Mark where platelets are.
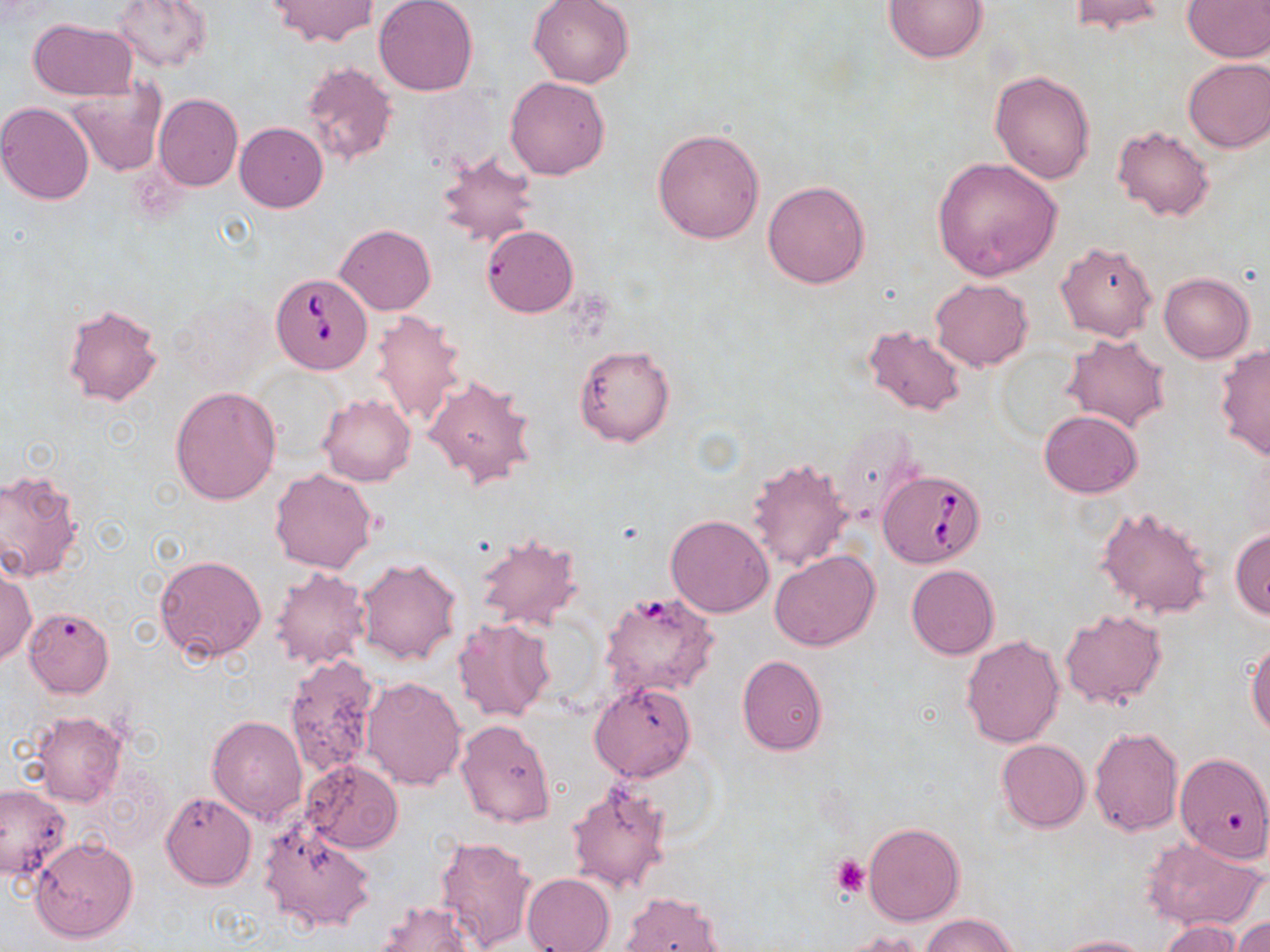
Approximate bounding boxes as named x1/y1/x2/y2 corners in pixels.
Platelets: (x1=831, y1=854, x2=871, y2=898).

Uninfected red blood cell locations: (x1=113, y1=0, x2=212, y2=71), (x1=264, y1=0, x2=378, y2=47), (x1=374, y1=0, x2=479, y2=97), (x1=528, y1=0, x2=634, y2=87), (x1=884, y1=0, x2=989, y2=64), (x1=1068, y1=0, x2=1165, y2=35), (x1=1183, y1=1, x2=1270, y2=61), (x1=28, y1=18, x2=138, y2=101), (x1=1182, y1=57, x2=1270, y2=153), (x1=302, y1=61, x2=398, y2=166), (x1=990, y1=69, x2=1095, y2=185), (x1=505, y1=76, x2=610, y2=179), (x1=64, y1=82, x2=166, y2=176), (x1=152, y1=93, x2=242, y2=191), (x1=0, y1=103, x2=96, y2=205), (x1=234, y1=122, x2=328, y2=212), (x1=1112, y1=124, x2=1214, y2=222), (x1=651, y1=127, x2=765, y2=244), (x1=432, y1=148, x2=539, y2=251), (x1=931, y1=157, x2=1062, y2=280), (x1=762, y1=180, x2=870, y2=288), (x1=337, y1=223, x2=435, y2=314), (x1=481, y1=225, x2=577, y2=317), (x1=1055, y1=240, x2=1158, y2=341), (x1=1158, y1=271, x2=1255, y2=362), (x1=931, y1=278, x2=1032, y2=370), (x1=61, y1=301, x2=162, y2=406), (x1=369, y1=309, x2=469, y2=430), (x1=862, y1=325, x2=967, y2=417), (x1=1062, y1=333, x2=1172, y2=433), (x1=1214, y1=343, x2=1270, y2=461), (x1=573, y1=345, x2=675, y2=447), (x1=423, y1=372, x2=537, y2=490), (x1=170, y1=386, x2=282, y2=506), (x1=318, y1=393, x2=416, y2=487), (x1=1040, y1=409, x2=1142, y2=498), (x1=832, y1=423, x2=924, y2=524), (x1=747, y1=457, x2=854, y2=573), (x1=269, y1=469, x2=378, y2=573), (x1=0, y1=470, x2=85, y2=582), (x1=1094, y1=504, x2=1214, y2=619), (x1=665, y1=515, x2=774, y2=618), (x1=1230, y1=528, x2=1270, y2=620), (x1=474, y1=532, x2=583, y2=629), (x1=769, y1=551, x2=879, y2=651), (x1=155, y1=554, x2=268, y2=664), (x1=355, y1=556, x2=462, y2=666), (x1=0, y1=563, x2=35, y2=666), (x1=906, y1=565, x2=999, y2=660), (x1=270, y1=567, x2=370, y2=669), (x1=598, y1=593, x2=718, y2=699), (x1=22, y1=606, x2=115, y2=699), (x1=1059, y1=609, x2=1167, y2=710), (x1=452, y1=618, x2=556, y2=723), (x1=960, y1=634, x2=1064, y2=748), (x1=1247, y1=638, x2=1270, y2=738), (x1=736, y1=655, x2=828, y2=754), (x1=284, y1=657, x2=377, y2=779), (x1=361, y1=676, x2=467, y2=791), (x1=589, y1=681, x2=696, y2=781), (x1=32, y1=711, x2=127, y2=806), (x1=207, y1=714, x2=307, y2=825), (x1=455, y1=718, x2=555, y2=828), (x1=1088, y1=727, x2=1184, y2=837), (x1=997, y1=739, x2=1090, y2=832), (x1=1176, y1=754, x2=1268, y2=874), (x1=301, y1=759, x2=402, y2=853), (x1=566, y1=780, x2=671, y2=895), (x1=0, y1=783, x2=70, y2=881), (x1=161, y1=792, x2=255, y2=891), (x1=259, y1=819, x2=377, y2=933), (x1=863, y1=822, x2=964, y2=926), (x1=436, y1=836, x2=537, y2=949), (x1=1141, y1=836, x2=1267, y2=932), (x1=30, y1=837, x2=138, y2=944), (x1=522, y1=873, x2=615, y2=952), (x1=617, y1=890, x2=728, y2=951), (x1=374, y1=900, x2=479, y2=952), (x1=921, y1=912, x2=1017, y2=952), (x1=1232, y1=914, x2=1270, y2=952), (x1=1158, y1=920, x2=1244, y2=952), (x1=838, y1=930, x2=927, y2=952), (x1=1050, y1=934, x2=1154, y2=952). Babesia divergens-infected red blood cell locations: (x1=270, y1=271, x2=374, y2=374), (x1=878, y1=469, x2=985, y2=567). Slide-level diagnosis: Babesia divergens. Image is 1270×952 pixels. Single field of view. Thin blood smear. Light microscopy. May-Grünwald-Giemsa-stained preparation. Captured at 1000x magnification.